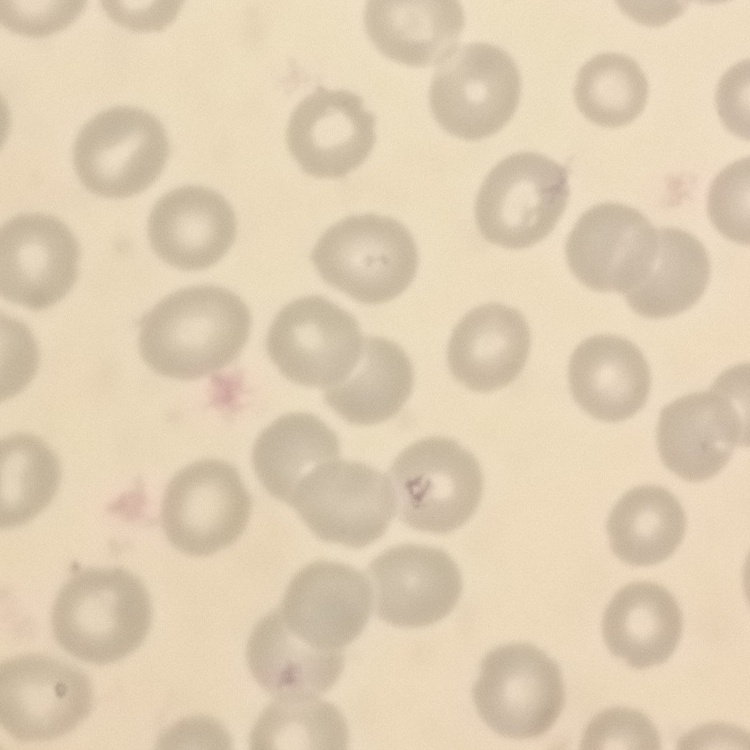
Summary:
  - Red blood cell morphology: no rouleaux formation
  - Preparation: thin blood smear
  - Stain: Field's or Giemsa
  - Image type: square crop of a larger photomicrograph